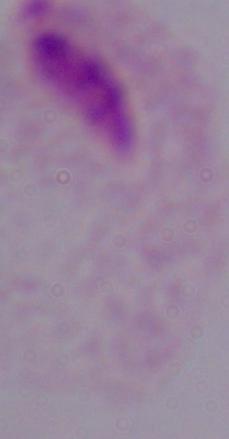

magnification: 1000x
modality: micrograph
identification: trichomonad